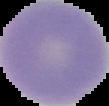 From a thin blood smear. The area outside the segmented cell region is set to black. Image is 109×106 pixels. Malaria status: uninfected.